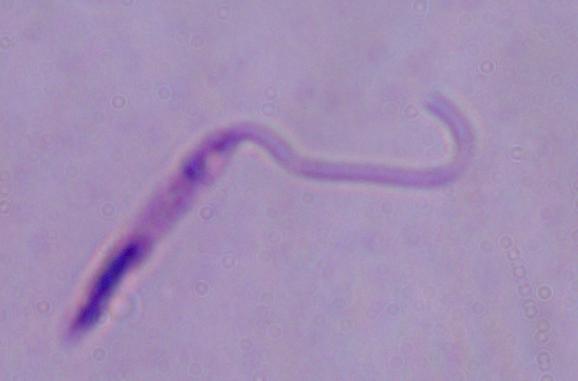
Summary:
  - Identification: Leishmania
  - Magnification: 1000x
  - Modality: micrograph